Look for parasitized red blood cells.
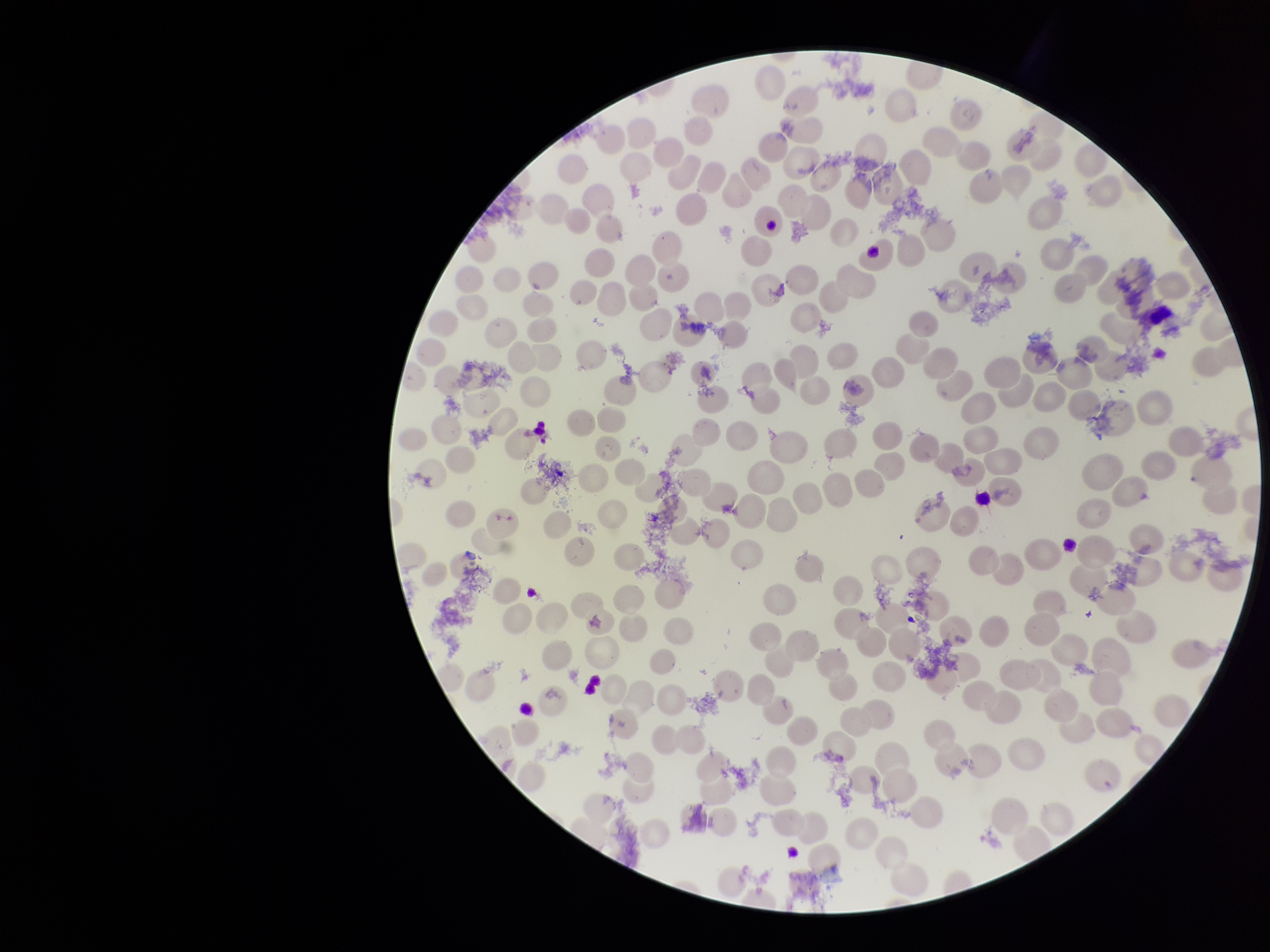

None detected.

stain: Giemsa
species_reported_for_this_patient: Plasmodium vivax
red_blood_cell_count: 230
image_size: 1270×952 pixels
preparation: thin smear
capture: smartphone photograph through the microscope eyepiece
parasitized_red_blood_cell_count: 0
patient_malaria_status: positive
field_of_view: one from this slide